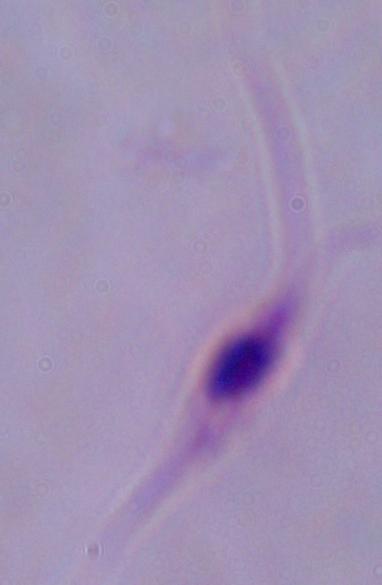 Captured at 1000x magnification. Micrograph. A Leishmania parasite is shown.